Identify the preparation type.
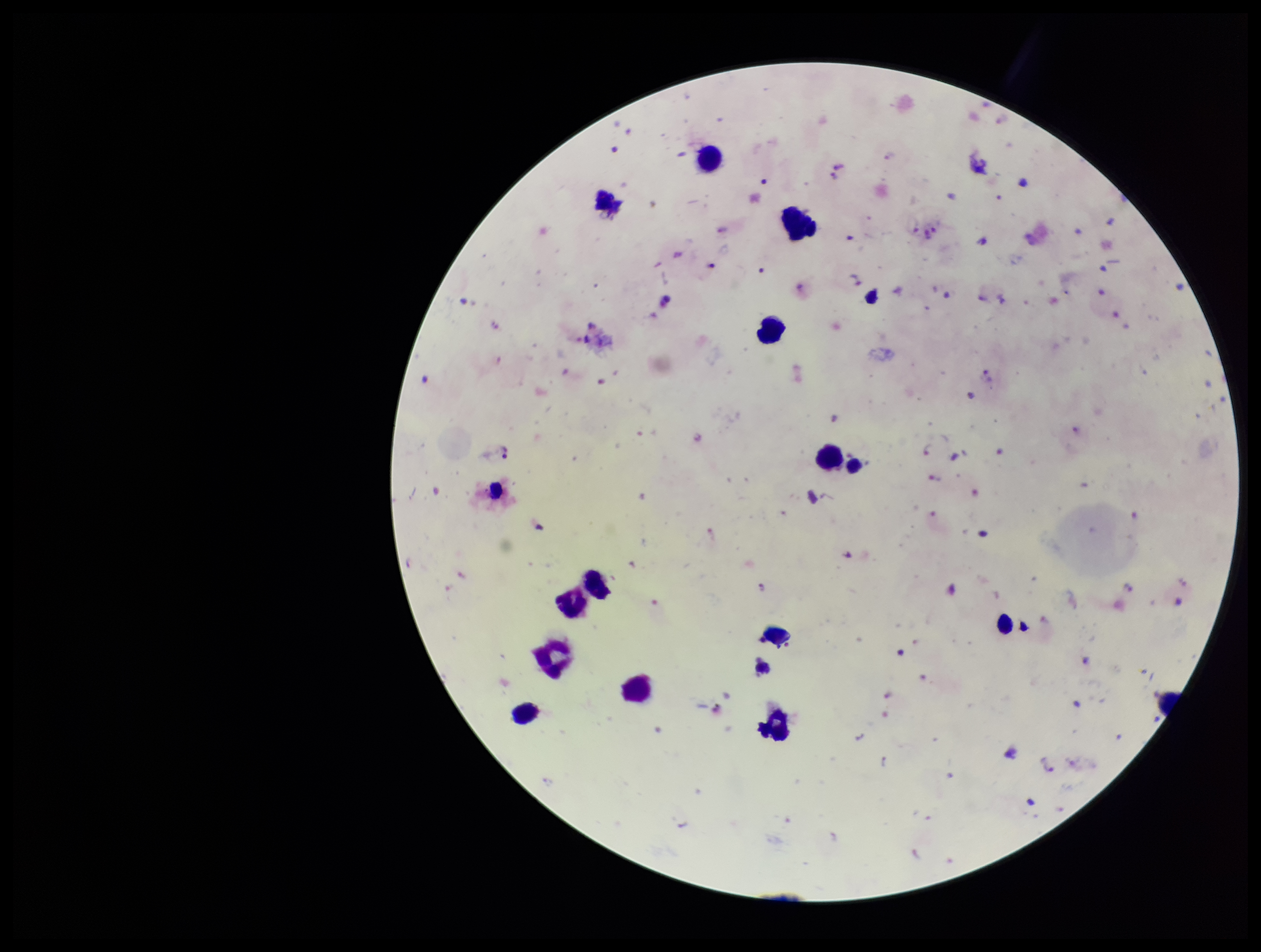

A thick smear.

Leukocyte count: 12. Photographed through the microscope eyepiece with a smartphone camera. Plasmodium parasites: detected. One field from this slide. Species reported for this patient: Plasmodium falciparum. Parasite count: 45. Image is 1261×952 pixels. Stained with Giemsa. Patient malaria status: infected.